Locate every malaria parasite.
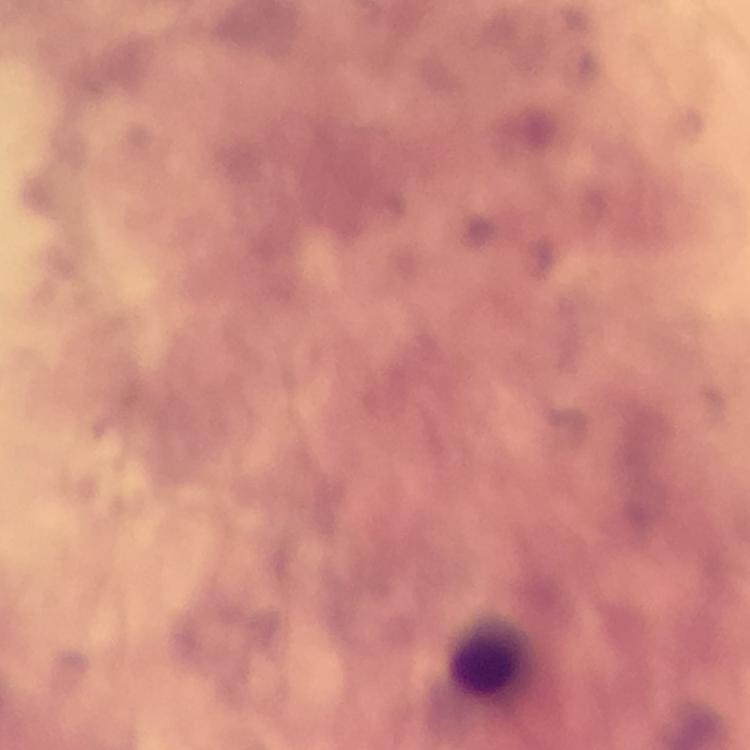

No malaria parasites seen.

Approximate object centers, in pixels from the top-left corner. Leukocyte locations: (x=490, y=659). Thick smear. 100x magnification. From a diagnostic examination for malaria. Immersion oil applied. A crop from one field of view. Smartphone photograph taken through a microscope. Image is 750×750 pixels. Giemsa-stained preparation.